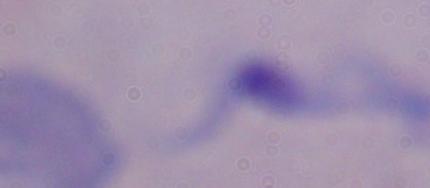
{
  "modality": "photomicrograph",
  "identification": "trypanosome",
  "magnification": "1000x"
}